Locate every blood parasite and identify its species.
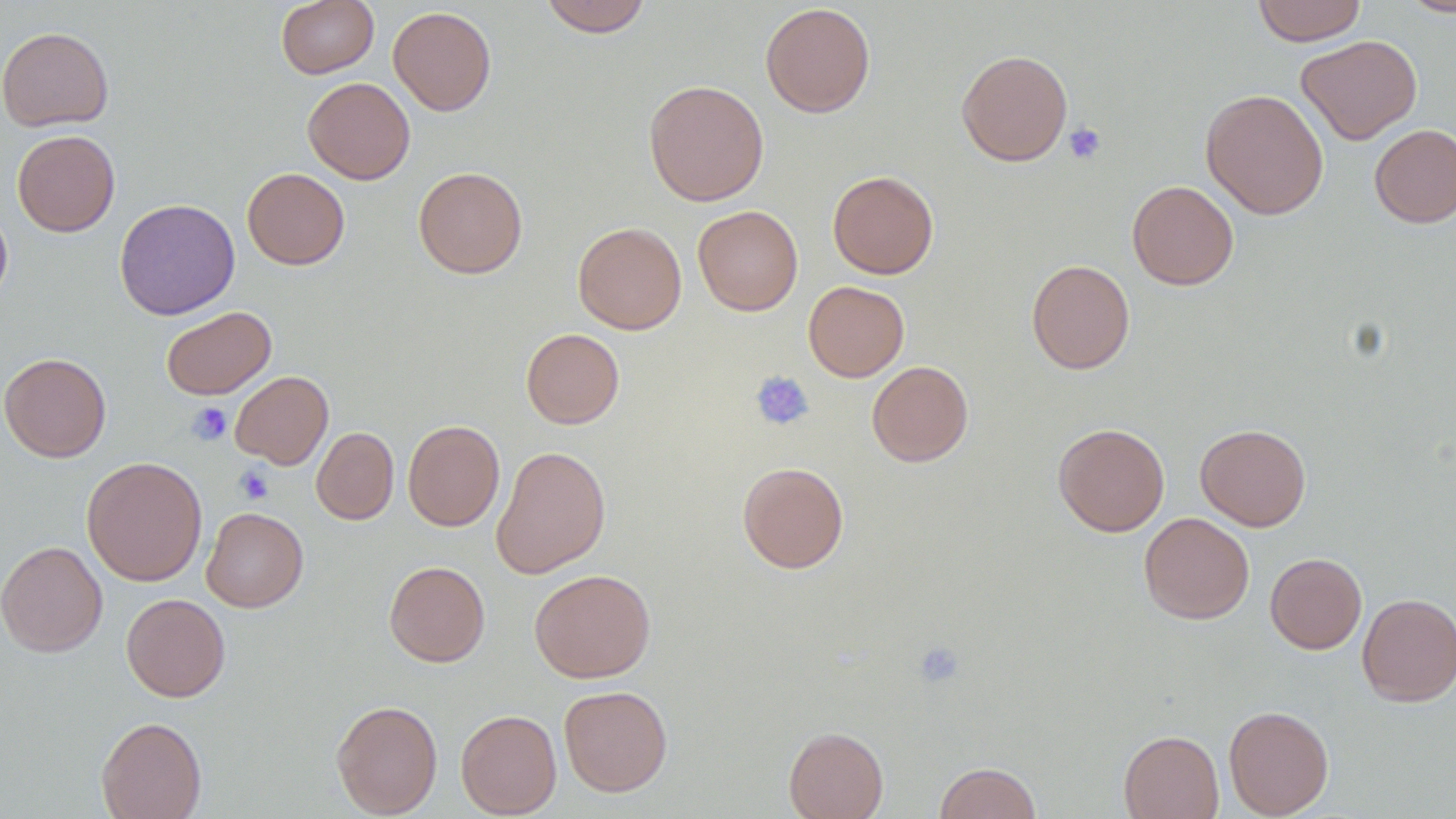

No blood parasites seen.

slide-level diagnosis = negative for blood parasites
uninfected red blood cell locations = approximate bounding boxes as (x1,y1)-(x2,y2) corner pairs in pixels: (276,0)-(379,78), (538,0)-(652,37), (1251,0)-(1367,46), (1399,0)-(1456,18), (760,2)-(876,117), (388,6)-(496,116), (0,26)-(114,132), (1296,34)-(1423,145), (956,49)-(1073,166), (303,77)-(415,184), (643,79)-(769,206), (1200,88)-(1329,220), (1369,124)-(1456,227), (12,129)-(120,237), (413,166)-(528,279), (242,168)-(350,270), (827,170)-(939,279), (1127,180)-(1239,290), (114,198)-(240,320), (0,203)-(13,311), (692,205)-(803,316), (572,221)-(687,334), (1026,259)-(1135,374), (803,281)-(909,382), (160,306)-(276,400), (521,328)-(624,429), (0,352)-(111,462), (867,361)-(973,466), (230,371)-(333,469), (403,420)-(504,531), (1053,423)-(1170,536), (1195,423)-(1311,531), (311,426)-(399,524), (490,444)-(611,579), (82,456)-(207,586), (737,461)-(849,573), (201,507)-(308,612), (1139,512)-(1255,625), (0,540)-(108,657), (1265,552)-(1367,654), (384,561)-(490,667), (529,569)-(656,683), (121,593)-(230,702), (1357,593)-(1456,706), (559,685)-(673,797), (331,699)-(442,818), (1223,705)-(1334,818), (455,709)-(561,818), (95,716)-(207,819), (783,726)-(889,819), (1118,729)-(1224,819), (933,761)-(1042,819)
platelet locations = approximate bounding boxes as (x1,y1)-(x2,y2) corner pairs in pixels: (1063,123)-(1106,164), (750,370)-(814,431), (187,402)-(232,445), (235,465)-(274,504), (913,641)-(965,689)
preparation = thin blood film
image size = 1456×819 pixels
modality = light microscopy
magnification = 1000x
field of view = single